Locate and identify every blood parasite.
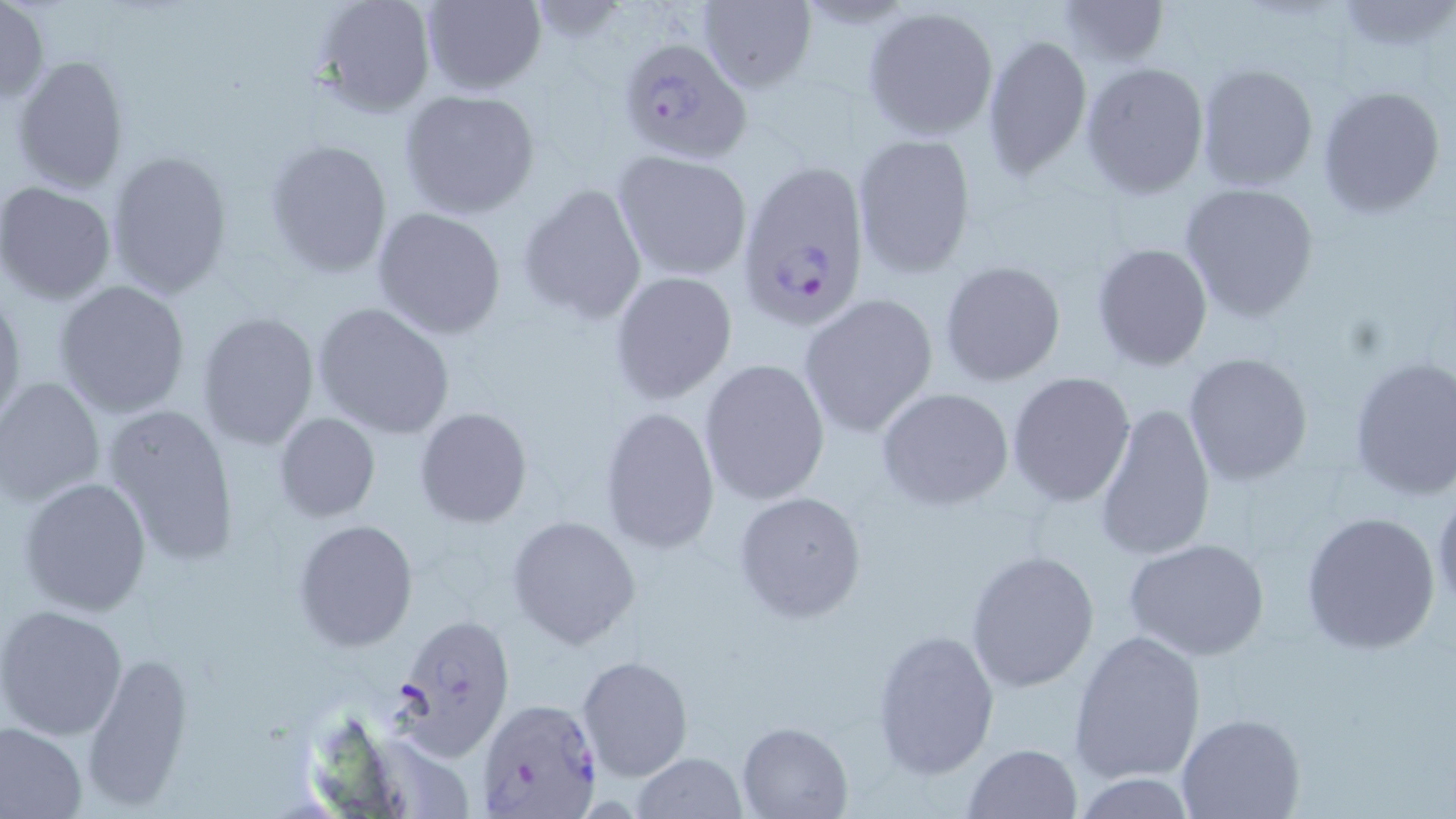
Approximate bounding boxes as named x1/y1/x2/y2 corners in pixels.
Plasmodium falciparum-infected red blood cells: (x1=619, y1=38, x2=752, y2=164), (x1=741, y1=162, x2=875, y2=331), (x1=392, y1=611, x2=517, y2=759), (x1=477, y1=697, x2=602, y2=816).
No Plasmodium ovale, Plasmodium malariae, Plasmodium vivax, Babesia divergens, or Trypanosoma brucei observed.

Uninfected red blood cell locations: (x1=313, y1=0, x2=433, y2=116), (x1=417, y1=0, x2=547, y2=95), (x1=1056, y1=0, x2=1170, y2=66), (x1=1337, y1=1, x2=1455, y2=53), (x1=0, y1=2, x2=50, y2=104), (x1=696, y1=2, x2=816, y2=94), (x1=862, y1=7, x2=999, y2=139), (x1=981, y1=32, x2=1092, y2=180), (x1=11, y1=53, x2=131, y2=194), (x1=1081, y1=62, x2=1211, y2=198), (x1=1195, y1=62, x2=1320, y2=192), (x1=1315, y1=84, x2=1446, y2=219), (x1=397, y1=88, x2=541, y2=218), (x1=852, y1=131, x2=975, y2=277), (x1=266, y1=139, x2=394, y2=277), (x1=106, y1=151, x2=233, y2=298), (x1=612, y1=151, x2=752, y2=281), (x1=0, y1=182, x2=117, y2=305), (x1=1179, y1=182, x2=1320, y2=322), (x1=519, y1=184, x2=646, y2=324), (x1=373, y1=207, x2=507, y2=339), (x1=1092, y1=242, x2=1213, y2=371), (x1=940, y1=261, x2=1067, y2=387), (x1=611, y1=271, x2=737, y2=402), (x1=53, y1=280, x2=191, y2=417), (x1=0, y1=292, x2=24, y2=425), (x1=799, y1=292, x2=941, y2=436), (x1=312, y1=302, x2=455, y2=440), (x1=196, y1=311, x2=321, y2=452), (x1=1182, y1=352, x2=1314, y2=486), (x1=1347, y1=355, x2=1456, y2=500), (x1=698, y1=358, x2=831, y2=505), (x1=1007, y1=371, x2=1136, y2=507), (x1=0, y1=377, x2=105, y2=507), (x1=875, y1=386, x2=1015, y2=509), (x1=1094, y1=400, x2=1217, y2=562), (x1=102, y1=402, x2=240, y2=566), (x1=599, y1=406, x2=720, y2=553), (x1=414, y1=407, x2=532, y2=528), (x1=273, y1=413, x2=382, y2=524), (x1=17, y1=475, x2=153, y2=615), (x1=731, y1=488, x2=867, y2=623), (x1=1431, y1=488, x2=1455, y2=618), (x1=1300, y1=510, x2=1442, y2=653), (x1=507, y1=516, x2=641, y2=649), (x1=293, y1=519, x2=417, y2=652), (x1=1124, y1=537, x2=1272, y2=662), (x1=966, y1=549, x2=1100, y2=692), (x1=0, y1=603, x2=129, y2=741), (x1=870, y1=628, x2=1001, y2=780), (x1=1068, y1=629, x2=1207, y2=784), (x1=79, y1=650, x2=192, y2=808), (x1=577, y1=655, x2=692, y2=782), (x1=1177, y1=713, x2=1306, y2=819), (x1=736, y1=720, x2=854, y2=818), (x1=0, y1=722, x2=87, y2=818), (x1=961, y1=742, x2=1083, y2=819), (x1=629, y1=752, x2=748, y2=819), (x1=1075, y1=774, x2=1199, y2=817). Slide-level diagnosis: Plasmodium falciparum. Image is 1456×819 pixels. Light microscopy. Thin blood smear. May-Grünwald-Giemsa-stained preparation. Single field of view. Captured at 1000x magnification.